Report the malaria status of this cell.
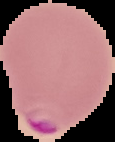

Parasitized.

From a thin blood smear. Image is 115×142 pixels. Cell region segmented out of the field of view; the surrounding area is masked to black.